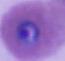
Photomicrograph. A Plasmodium parasite is seen. 400x or 1000x magnification.